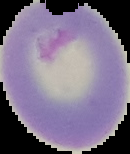

Image is 130×154 pixels. Malaria status: uninfected. The area outside the segmented cell region is set to black. From a thin blood smear.